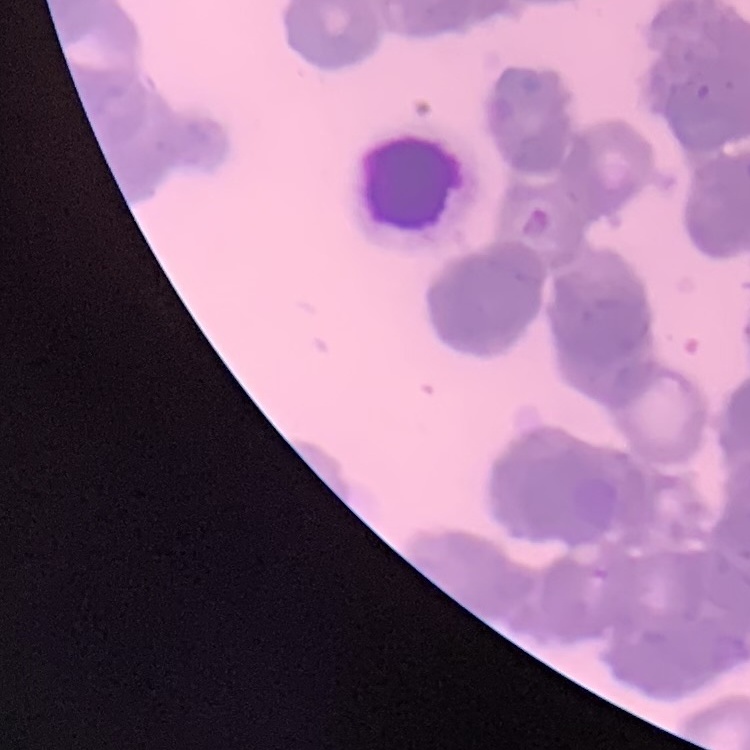

Summary:
  - Red blood cell morphology: rouleaux formation
  - Preparation: thin blood smear
  - Image type: one tile cut from a larger photomicrograph
  - Stain: Field's or Giemsa